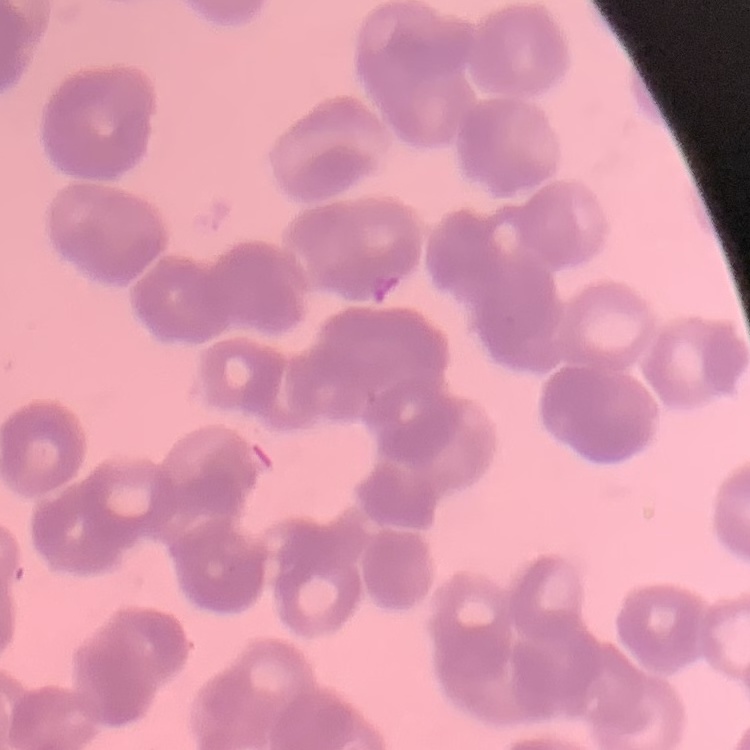 The erythrocytes show rouleaux formation. Square crop of a larger photomicrograph. Thin blood film. Stained with either Field's or Giemsa.